Give the position of every Plasmodium parasite visible.
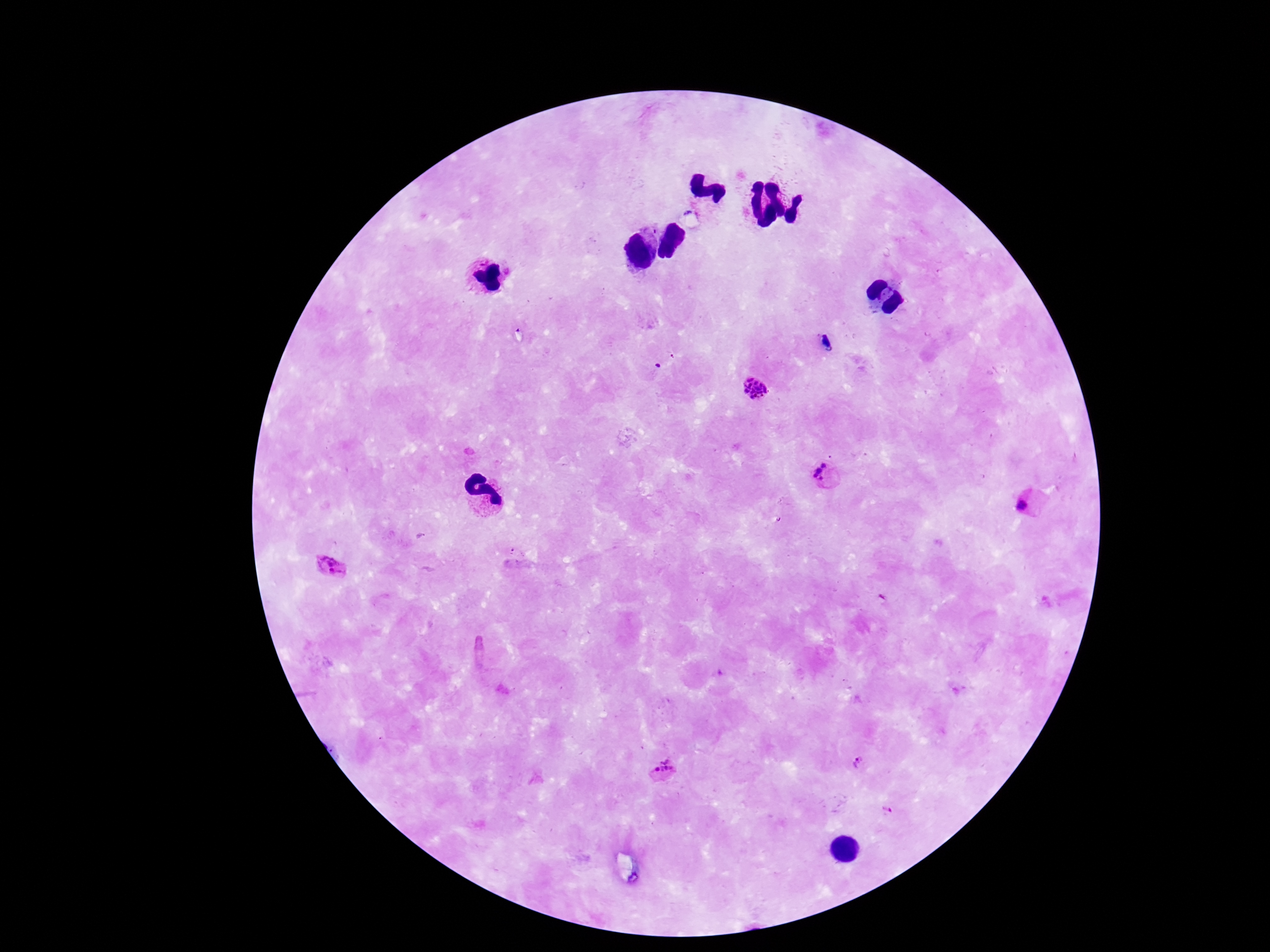

Approximate object centers, in pixels from the top-left corner.
Plasmodium parasites: (x=826, y=344), (x=754, y=390), (x=831, y=475), (x=1029, y=502), (x=330, y=572), (x=858, y=764), (x=665, y=773), (x=886, y=813).

{
  "patient_malaria_status": "positive",
  "field_of_view": "one from this slide",
  "capture": "smartphone camera through the microscope eyepiece",
  "stain": "Giemsa",
  "magnification": "100x",
  "image_size": "1270×952 pixels",
  "preparation": "thick blood film"
}